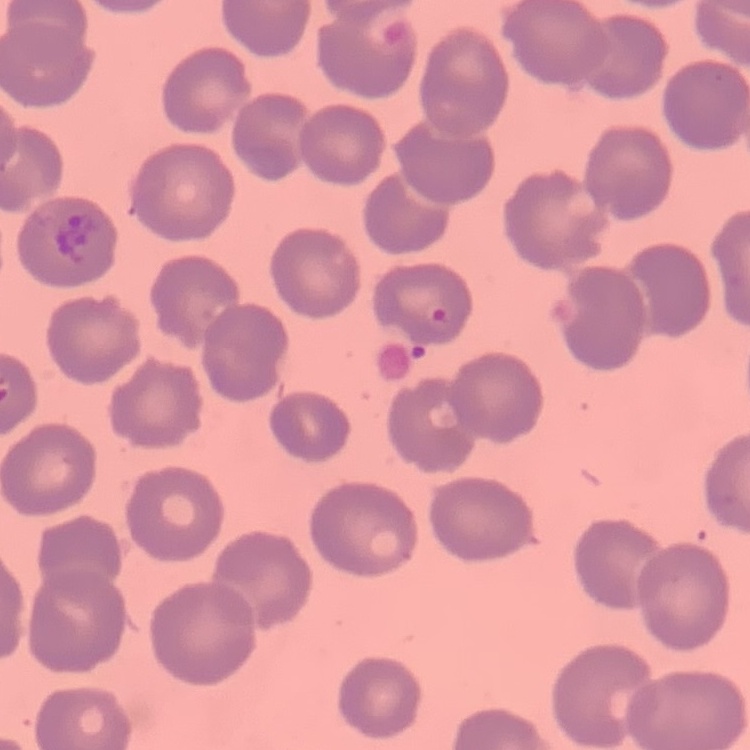
red blood cell morphology = no rouleaux formation
preparation = thin peripheral smear
stain = Field's or Giemsa
image type = one tile cut from a larger photomicrograph